Identify the parasite.
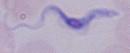
This is a trypanosome.

Summary:
  - Modality: photomicrograph
  - Magnification: 1000x